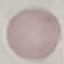

Summary:
  - Malaria status: uninfected
  - Preparation: thin blood film
  - Stain: Giemsa
  - Capture: smartphone through the microscope eyepiece
  - Image type: automatically extracted cell patch, resized to 64 × 64 pixels